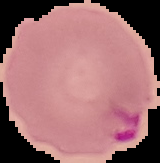

Summary:
  - Result: malaria parasites identified
  - Image type: segmented cell region with the area outside set to black
  - Image size: 160×163 pixels
  - Preparation: thin blood smear